State which parasite is depicted.
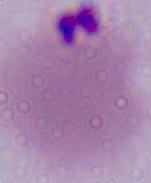

This is Plasmodium.

Summary:
  - Modality: photomicrograph
  - Magnification: 400x or 1000x